Describe the morphology of the erythrocytes.
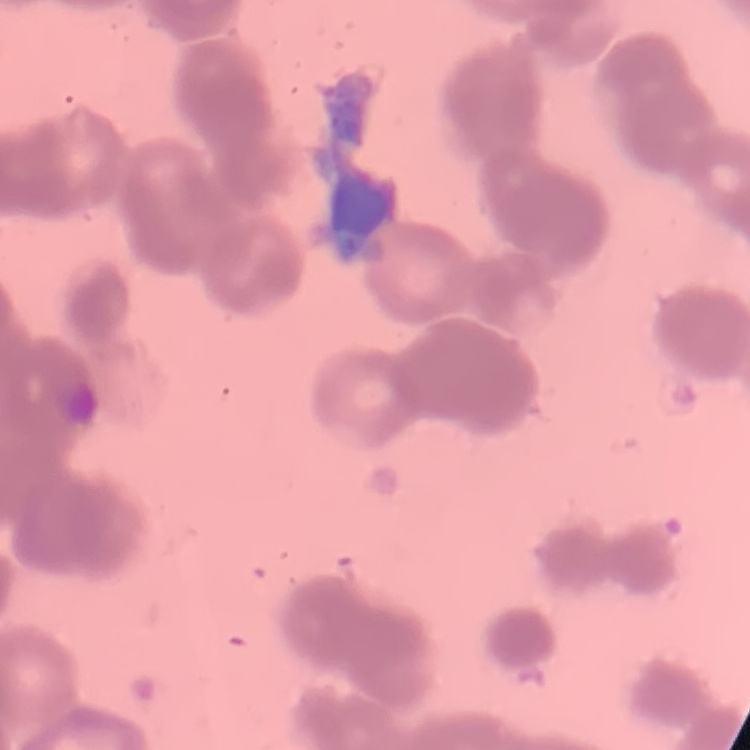
They show rouleaux formation.

Square crop of a larger photomicrograph. Thin peripheral smear. Field's or Giemsa stain.